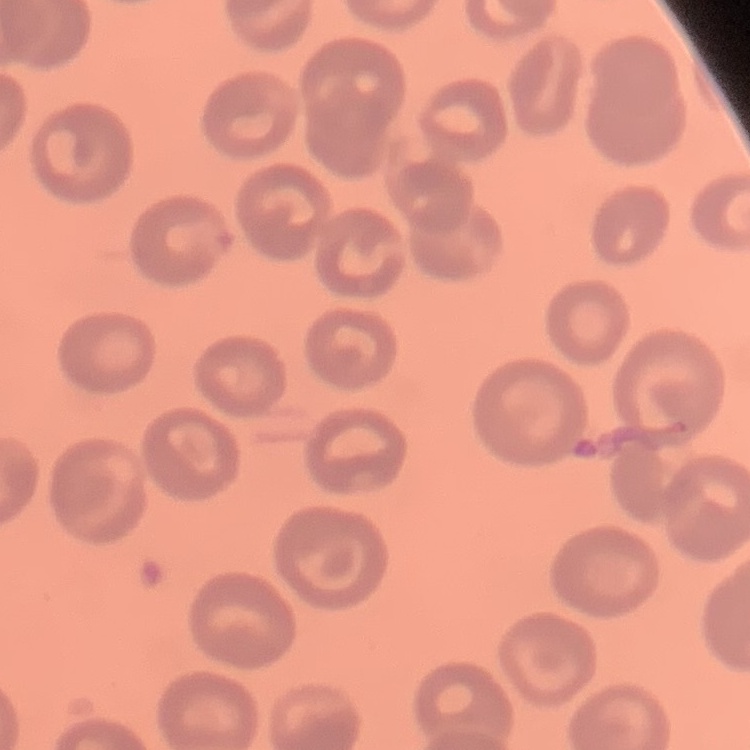
The erythrocytes show no rouleaux formation. Thin blood smear. Field's or Giemsa stain. Square crop of a larger photomicrograph.